Outline each blood parasite and name the species.
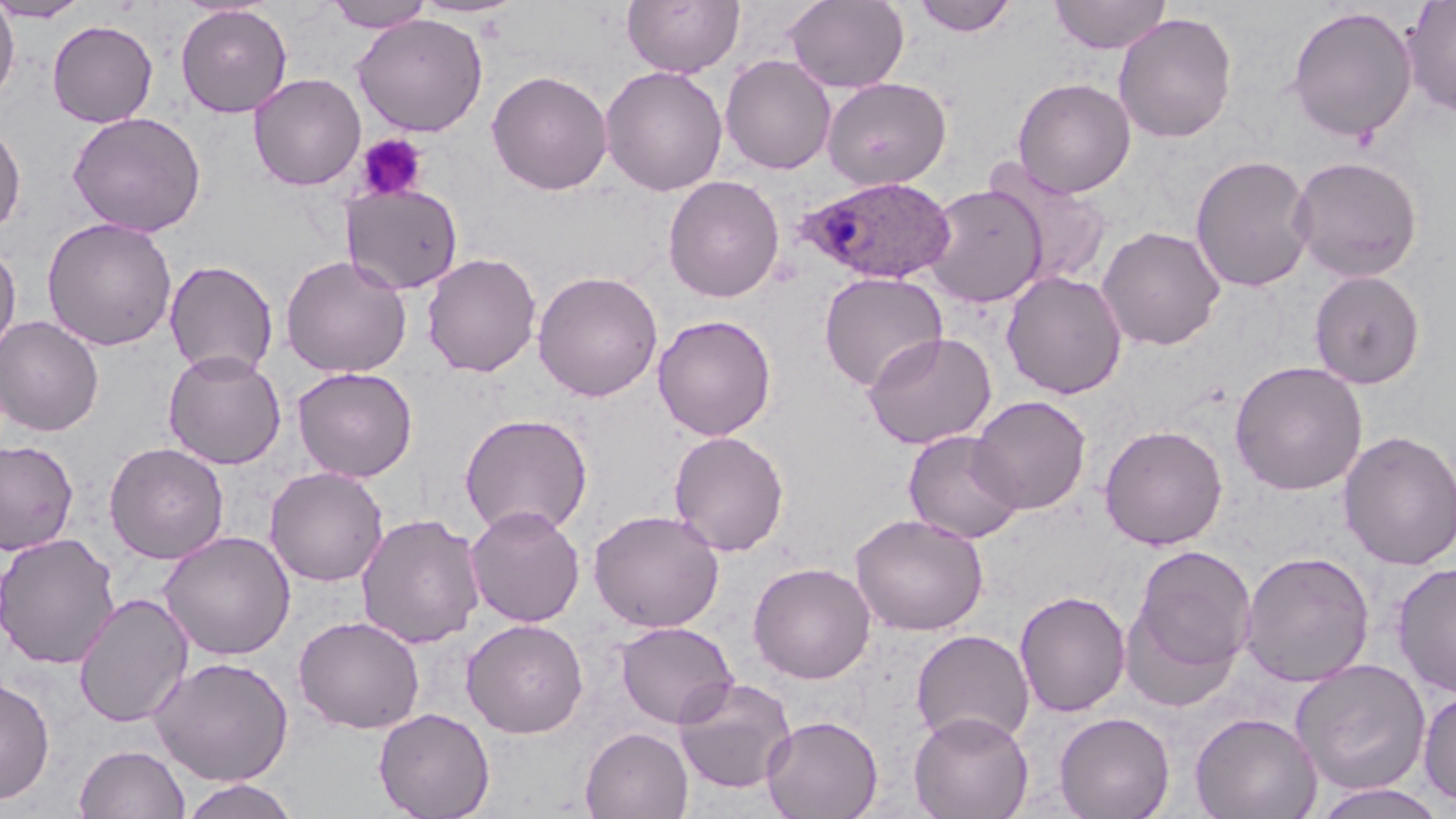

Approximate bounding boxes as (x1, y1, x2, y2) in pixels.
Plasmodium ovale-infected red blood cells: (799, 176, 956, 284).
No Plasmodium falciparum, Plasmodium malariae, Plasmodium vivax, Babesia divergens, or Trypanosoma brucei observed.

slide-level diagnosis = Plasmodium ovale
field of view = one of a larger specimen
magnification = 1000x
stain = May-Grünwald-Giemsa
preparation = thin blood film
image size = 1456×819 pixels
modality = optical microscopy
uninfected red blood cell locations = approximate bounding boxes as (x1, y1, x2, y2) in pixels: (0, 0, 92, 22), (411, 0, 527, 19), (622, 0, 744, 77), (784, 0, 909, 92), (911, 0, 1018, 37), (1049, 0, 1172, 54), (323, 1, 435, 32), (1400, 1, 1456, 118), (0, 2, 20, 104), (176, 4, 292, 118), (1286, 6, 1418, 142), (1113, 12, 1238, 143), (352, 14, 488, 136), (48, 19, 158, 128), (720, 55, 836, 174), (600, 65, 727, 196), (487, 70, 613, 195), (248, 73, 366, 191), (822, 77, 951, 190), (1012, 77, 1136, 198), (67, 111, 206, 237), (0, 120, 26, 236), (1190, 154, 1316, 293), (1289, 155, 1424, 283), (985, 164, 1115, 292), (663, 175, 785, 302), (340, 183, 465, 295), (922, 184, 1048, 307), (42, 217, 177, 351), (1096, 225, 1226, 351), (0, 240, 21, 360), (421, 252, 541, 377), (280, 255, 412, 378), (164, 259, 279, 379), (533, 270, 663, 402), (1001, 270, 1128, 399), (1309, 270, 1426, 390), (818, 272, 948, 391), (652, 314, 777, 440), (0, 316, 104, 436), (863, 331, 997, 450), (163, 350, 287, 469), (1229, 360, 1368, 495), (292, 367, 418, 482), (970, 395, 1092, 514), (459, 413, 593, 537), (1099, 424, 1228, 550), (903, 429, 1026, 544), (1338, 429, 1456, 571), (668, 430, 789, 556), (0, 440, 79, 555), (103, 442, 229, 564), (265, 466, 388, 586), (465, 504, 586, 627), (588, 509, 725, 632), (356, 512, 485, 649), (850, 513, 988, 635), (159, 530, 296, 660), (0, 532, 120, 669), (1128, 543, 1256, 686), (1239, 550, 1375, 687), (1392, 561, 1456, 697), (748, 562, 876, 684), (1014, 590, 1131, 717), (73, 592, 194, 728), (294, 615, 425, 734), (461, 618, 589, 737), (615, 621, 738, 728), (911, 629, 1035, 746), (150, 656, 294, 786), (1291, 659, 1432, 796), (0, 676, 55, 804), (673, 677, 797, 795), (1418, 687, 1456, 807), (373, 707, 495, 819), (909, 711, 1034, 819), (1054, 711, 1175, 819), (1190, 711, 1322, 819), (761, 714, 883, 819), (581, 727, 694, 819), (74, 744, 190, 819), (179, 777, 299, 819), (1310, 783, 1449, 819)
platelet locations = approximate bounding boxes as (x1, y1, x2, y2) in pixels: (355, 133, 428, 202)